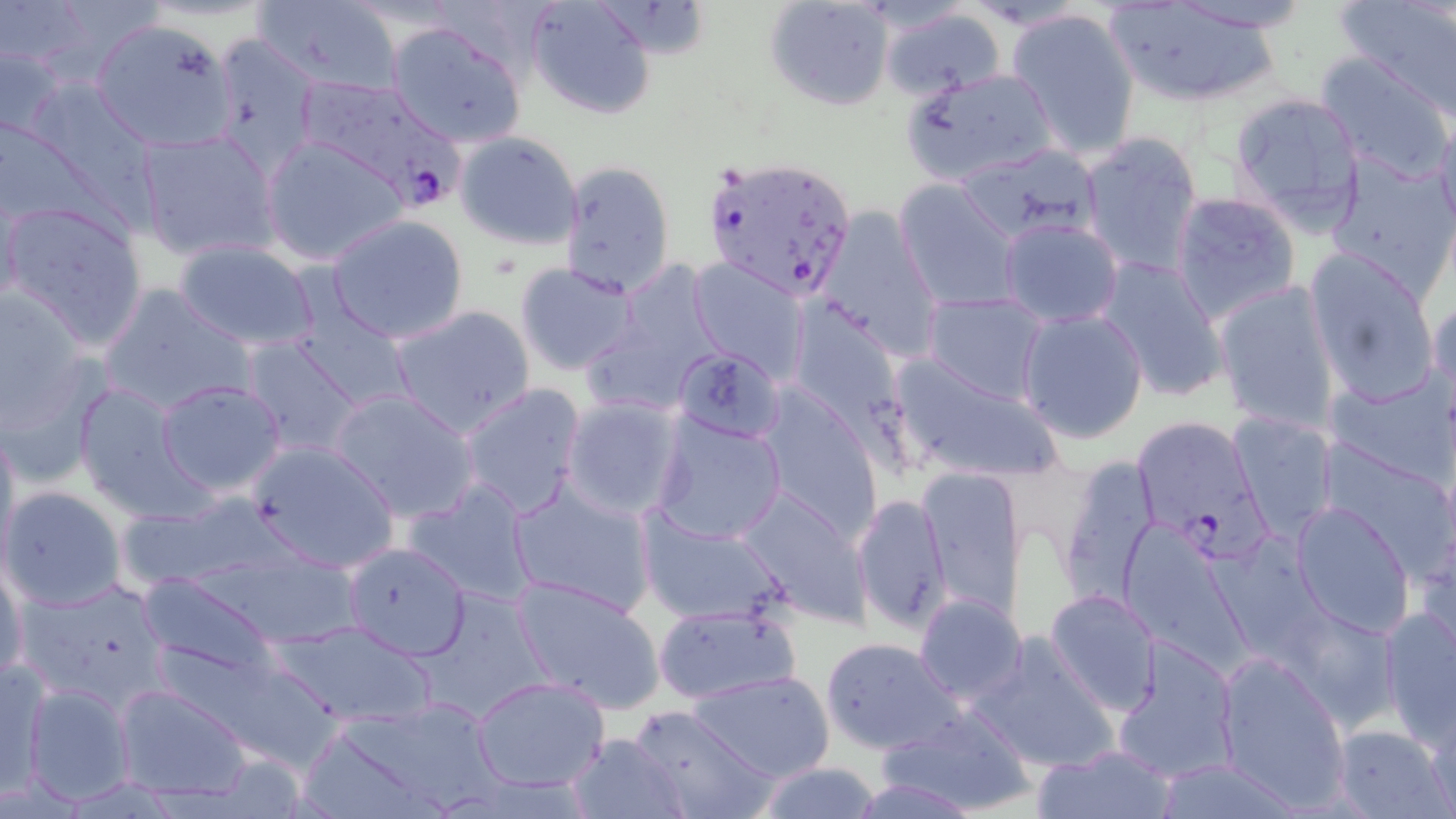
Plasmodium falciparum-infected red blood cell locations = approximate bounding boxes as named x1/y1/x2/y2 corners in pixels: (x1=292, y1=74, x2=464, y2=207), (x1=704, y1=154, x2=860, y2=301), (x1=1130, y1=413, x2=1265, y2=556)
slide-level diagnosis = Plasmodium falciparum
magnification = 1000x
field of view = single
uninfected red blood cell locations = approximate bounding boxes as named x1/y1/x2/y2 corners in pixels: (x1=526, y1=0, x2=658, y2=120), (x1=763, y1=0, x2=895, y2=111), (x1=254, y1=1, x2=402, y2=93), (x1=1158, y1=1, x2=1317, y2=35), (x1=1335, y1=1, x2=1456, y2=123), (x1=1102, y1=2, x2=1284, y2=108), (x1=1006, y1=6, x2=1140, y2=160), (x1=879, y1=7, x2=1008, y2=99), (x1=90, y1=17, x2=235, y2=149), (x1=386, y1=21, x2=525, y2=148), (x1=207, y1=33, x2=321, y2=178), (x1=1, y1=41, x2=71, y2=143), (x1=1313, y1=51, x2=1455, y2=178), (x1=900, y1=68, x2=1056, y2=185), (x1=42, y1=84, x2=178, y2=249), (x1=1229, y1=91, x2=1369, y2=232), (x1=1434, y1=109, x2=1456, y2=236), (x1=134, y1=130, x2=279, y2=262), (x1=453, y1=130, x2=585, y2=249), (x1=1079, y1=130, x2=1203, y2=277), (x1=261, y1=136, x2=408, y2=267), (x1=956, y1=144, x2=1102, y2=246), (x1=1326, y1=153, x2=1456, y2=297), (x1=556, y1=158, x2=676, y2=296), (x1=893, y1=181, x2=1021, y2=310), (x1=1170, y1=192, x2=1300, y2=325), (x1=2, y1=199, x2=148, y2=348), (x1=815, y1=204, x2=943, y2=361), (x1=326, y1=215, x2=469, y2=344), (x1=999, y1=216, x2=1124, y2=329), (x1=170, y1=238, x2=320, y2=352), (x1=1304, y1=249, x2=1440, y2=407), (x1=1095, y1=255, x2=1230, y2=402), (x1=688, y1=257, x2=811, y2=383), (x1=514, y1=263, x2=640, y2=377), (x1=1213, y1=278, x2=1341, y2=433), (x1=0, y1=284, x2=95, y2=441), (x1=98, y1=284, x2=254, y2=416), (x1=922, y1=291, x2=1050, y2=404), (x1=1427, y1=292, x2=1455, y2=403), (x1=787, y1=298, x2=916, y2=455), (x1=290, y1=302, x2=414, y2=415), (x1=388, y1=305, x2=535, y2=439), (x1=1017, y1=307, x2=1149, y2=444), (x1=239, y1=336, x2=365, y2=459), (x1=672, y1=345, x2=785, y2=443), (x1=889, y1=353, x2=1062, y2=483), (x1=1326, y1=370, x2=1456, y2=484), (x1=155, y1=380, x2=288, y2=497), (x1=459, y1=382, x2=587, y2=518), (x1=71, y1=383, x2=207, y2=520), (x1=754, y1=384, x2=882, y2=543), (x1=329, y1=389, x2=479, y2=524), (x1=559, y1=397, x2=686, y2=520), (x1=1228, y1=412, x2=1336, y2=539), (x1=650, y1=414, x2=788, y2=543), (x1=0, y1=420, x2=21, y2=568), (x1=1318, y1=440, x2=1453, y2=569), (x1=243, y1=441, x2=400, y2=574), (x1=1058, y1=457, x2=1162, y2=605), (x1=917, y1=468, x2=1027, y2=623), (x1=403, y1=478, x2=539, y2=603), (x1=509, y1=478, x2=656, y2=617), (x1=731, y1=485, x2=871, y2=624), (x1=0, y1=486, x2=125, y2=612), (x1=853, y1=493, x2=953, y2=633), (x1=1291, y1=502, x2=1416, y2=637), (x1=637, y1=512, x2=791, y2=626), (x1=1125, y1=527, x2=1253, y2=680), (x1=341, y1=541, x2=473, y2=661), (x1=1231, y1=547, x2=1386, y2=727), (x1=1, y1=555, x2=27, y2=686), (x1=137, y1=573, x2=280, y2=684), (x1=511, y1=575, x2=666, y2=715), (x1=13, y1=578, x2=171, y2=712), (x1=1045, y1=589, x2=1163, y2=714), (x1=915, y1=594, x2=1026, y2=701), (x1=652, y1=602, x2=800, y2=706), (x1=1380, y1=604, x2=1456, y2=746), (x1=270, y1=618, x2=437, y2=726), (x1=969, y1=632, x2=1120, y2=775), (x1=1112, y1=636, x2=1241, y2=782), (x1=820, y1=637, x2=961, y2=754), (x1=1215, y1=653, x2=1351, y2=808), (x1=1, y1=659, x2=49, y2=802), (x1=687, y1=670, x2=835, y2=781), (x1=469, y1=676, x2=610, y2=791), (x1=113, y1=681, x2=255, y2=803), (x1=21, y1=683, x2=136, y2=806), (x1=305, y1=703, x2=508, y2=817), (x1=627, y1=705, x2=774, y2=819), (x1=880, y1=706, x2=1038, y2=816), (x1=1426, y1=715, x2=1456, y2=817), (x1=1332, y1=725, x2=1451, y2=817), (x1=564, y1=731, x2=689, y2=819), (x1=1033, y1=744, x2=1177, y2=819), (x1=1154, y1=759, x2=1303, y2=817), (x1=751, y1=761, x2=884, y2=819)
image size = 1456×819 pixels
preparation = thin blood smear
stain = May-Grünwald-Giemsa
modality = light microscopy